Name the cell type shown.
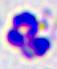

A leukocyte.

modality = photomicrograph
magnification = 400x